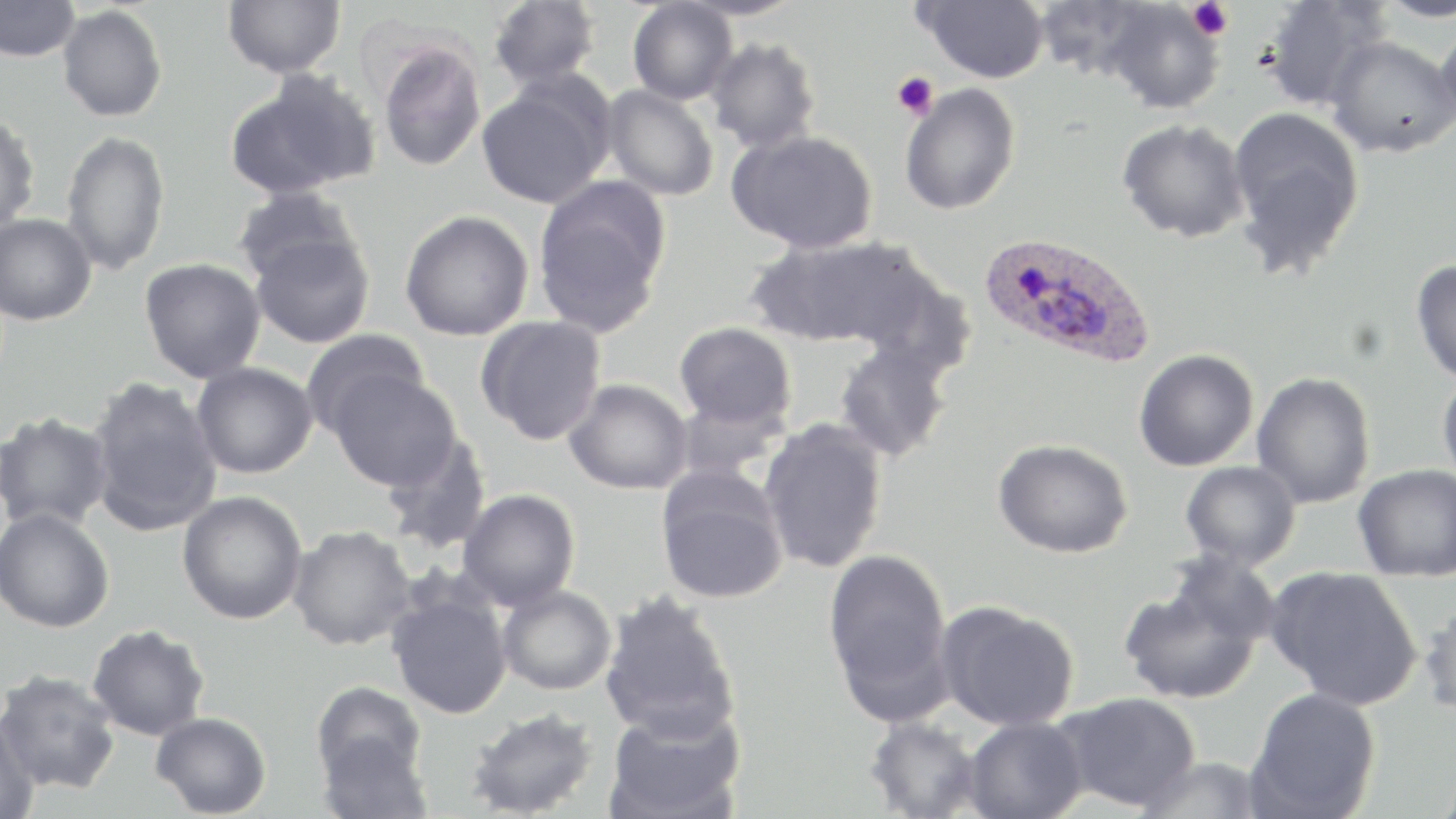

Approximate bounding boxes as [x1, y1, x2, y2] in pixels. Uninfected red blood cell locations: [0, 0, 81, 62], [223, 0, 346, 78], [488, 0, 601, 89], [915, 0, 1049, 83], [1033, 0, 1160, 82], [1256, 0, 1392, 113], [1375, 0, 1456, 22], [1099, 1, 1226, 114], [627, 2, 738, 105], [57, 5, 167, 122], [1434, 16, 1456, 140], [1325, 35, 1455, 158], [377, 36, 487, 172], [705, 36, 822, 154], [227, 72, 379, 198], [476, 78, 614, 208], [898, 82, 1021, 215], [601, 84, 719, 201], [1226, 105, 1366, 277], [0, 113, 41, 234], [1116, 118, 1251, 243], [728, 129, 879, 253], [60, 130, 170, 276], [532, 175, 672, 337], [232, 186, 363, 287], [399, 210, 534, 341], [0, 213, 98, 326], [248, 232, 375, 348], [745, 236, 922, 348], [139, 257, 266, 384], [1411, 258, 1456, 387], [850, 261, 979, 381], [475, 315, 606, 445], [674, 321, 797, 430], [300, 329, 430, 439], [832, 340, 954, 462], [1133, 349, 1259, 472], [191, 361, 318, 479], [328, 369, 461, 491], [1252, 371, 1376, 509], [1437, 371, 1456, 488], [85, 376, 223, 537], [564, 379, 693, 495], [673, 394, 791, 482], [1, 410, 114, 532], [758, 418, 889, 574], [378, 432, 492, 555], [993, 438, 1133, 558], [1180, 461, 1302, 570], [1353, 464, 1456, 582], [655, 466, 790, 605], [457, 488, 580, 610], [177, 491, 309, 624], [0, 507, 115, 633], [287, 525, 417, 650], [823, 547, 953, 716], [1163, 550, 1283, 647], [1265, 565, 1424, 711], [1118, 580, 1263, 705], [496, 584, 617, 695], [385, 586, 512, 720], [598, 590, 741, 742], [1419, 597, 1456, 721], [935, 600, 1080, 731], [87, 623, 211, 741], [0, 669, 121, 795], [311, 680, 428, 788], [1246, 687, 1381, 818], [1056, 691, 1202, 812], [603, 705, 746, 819], [465, 707, 600, 818], [150, 711, 272, 818], [0, 714, 40, 819], [964, 716, 1088, 819], [863, 717, 983, 819], [315, 730, 433, 818], [1133, 756, 1266, 818]. Plasmodium ovale-infected red blood cell locations: [978, 232, 1155, 368]. Platelet locations: [1187, 0, 1233, 40], [891, 72, 937, 120]. Slide-level diagnosis: Plasmodium ovale. Image is 1456×819 pixels. Single field of view. Light microscopy. 1000x magnification. Thin blood smear. May-Grünwald-Giemsa stain.